Assess the morphology of the red blood cells.
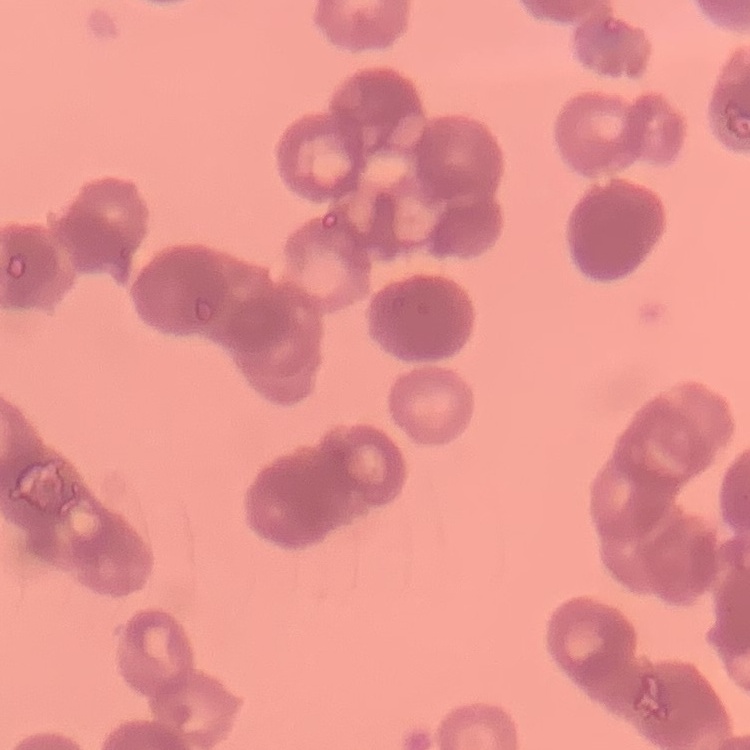

Rouleaux formation.

Summary:
  - Stain: Field's or Giemsa
  - Preparation: thin blood smear
  - Image type: one tile cut from a larger photomicrograph